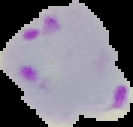

image size = 133×127 pixels
preparation = thin blood film
malaria status = parasitized
image type = segmented cell region on a black background